Locate every Plasmodium ovale-infected red blood cell.
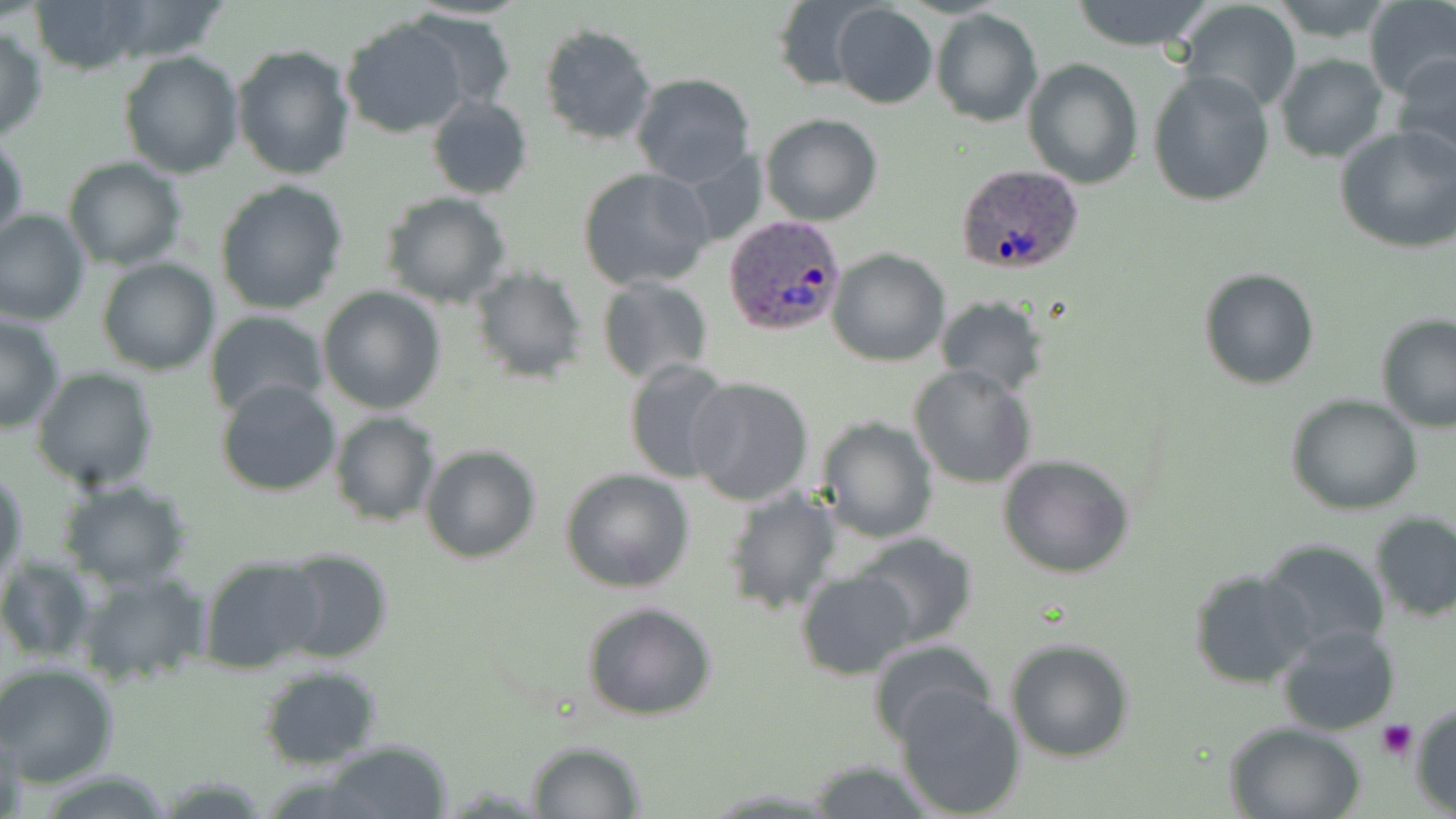
Approximate bounding boxes as (x1, y1, x2, y2) in pixels.
Plasmodium ovale-infected red blood cells: (953, 164, 1087, 277), (724, 215, 846, 336).

Summary:
  - Uninfected red blood cell locations: (29, 0, 155, 74), (92, 0, 233, 64), (769, 0, 874, 94), (1068, 0, 1217, 51), (1363, 0, 1456, 103), (1177, 1, 1302, 115), (831, 4, 938, 109), (931, 10, 1041, 127), (411, 12, 515, 115), (340, 17, 471, 139), (538, 23, 657, 146), (0, 25, 49, 144), (232, 42, 356, 180), (117, 51, 244, 178), (1276, 54, 1388, 163), (1393, 54, 1456, 170), (1023, 58, 1143, 189), (1147, 71, 1275, 209), (630, 73, 757, 188), (427, 96, 533, 200), (760, 113, 883, 226), (1335, 125, 1455, 253), (0, 131, 27, 252), (63, 156, 187, 271), (578, 166, 715, 291), (214, 181, 351, 317), (379, 192, 514, 309), (0, 208, 90, 328), (827, 248, 950, 367), (96, 257, 219, 375), (1198, 267, 1321, 390), (469, 269, 589, 383), (596, 276, 714, 387), (317, 285, 447, 413), (936, 296, 1050, 396), (204, 310, 328, 420), (0, 312, 66, 433), (1375, 315, 1456, 434), (622, 360, 737, 484), (908, 364, 1037, 487), (31, 367, 160, 492), (685, 376, 815, 506), (214, 377, 343, 497), (1285, 395, 1425, 515), (329, 411, 441, 526), (815, 415, 938, 543), (420, 445, 541, 564), (996, 452, 1137, 579), (1, 467, 27, 593), (560, 467, 695, 594), (56, 478, 194, 589), (719, 485, 844, 616), (1369, 510, 1456, 622), (851, 531, 979, 648), (1260, 539, 1391, 659), (275, 547, 395, 666), (0, 554, 95, 664), (197, 555, 327, 673), (1188, 568, 1317, 689), (72, 569, 210, 689), (794, 569, 917, 679), (581, 601, 718, 721), (1277, 625, 1400, 735), (866, 638, 996, 744), (1005, 638, 1135, 762), (0, 661, 120, 787), (258, 665, 383, 767), (896, 687, 1026, 818), (1410, 701, 1456, 815), (1226, 720, 1368, 819), (1, 729, 29, 819), (524, 740, 647, 818), (320, 741, 454, 818), (806, 759, 940, 818)
  - Platelet locations: (1377, 720, 1416, 759)
  - Slide-level diagnosis: Plasmodium ovale
  - Stain: May-Grünwald-Giemsa
  - Field of view: single
  - Preparation: thin blood film
  - Image size: 1456×819 pixels
  - Magnification: 1000x
  - Modality: optical microscopy